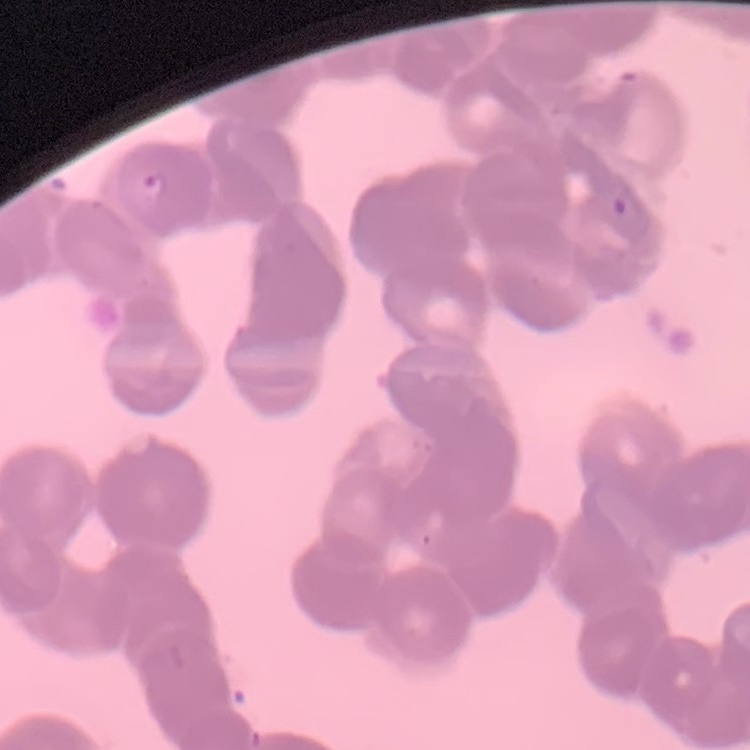
The red blood cells exhibit rouleaux formation. Square crop of a larger photomicrograph. Thin blood film. Field's or Giemsa stain.